Report the malaria status of this cell.
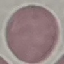

It is uninfected.

stain = Giemsa
capture = smartphone through the microscope eyepiece
preparation = thin blood smear
image type = automatically extracted cell patch, resized to 64 × 64 pixels